Outline each blood parasite and name the species.
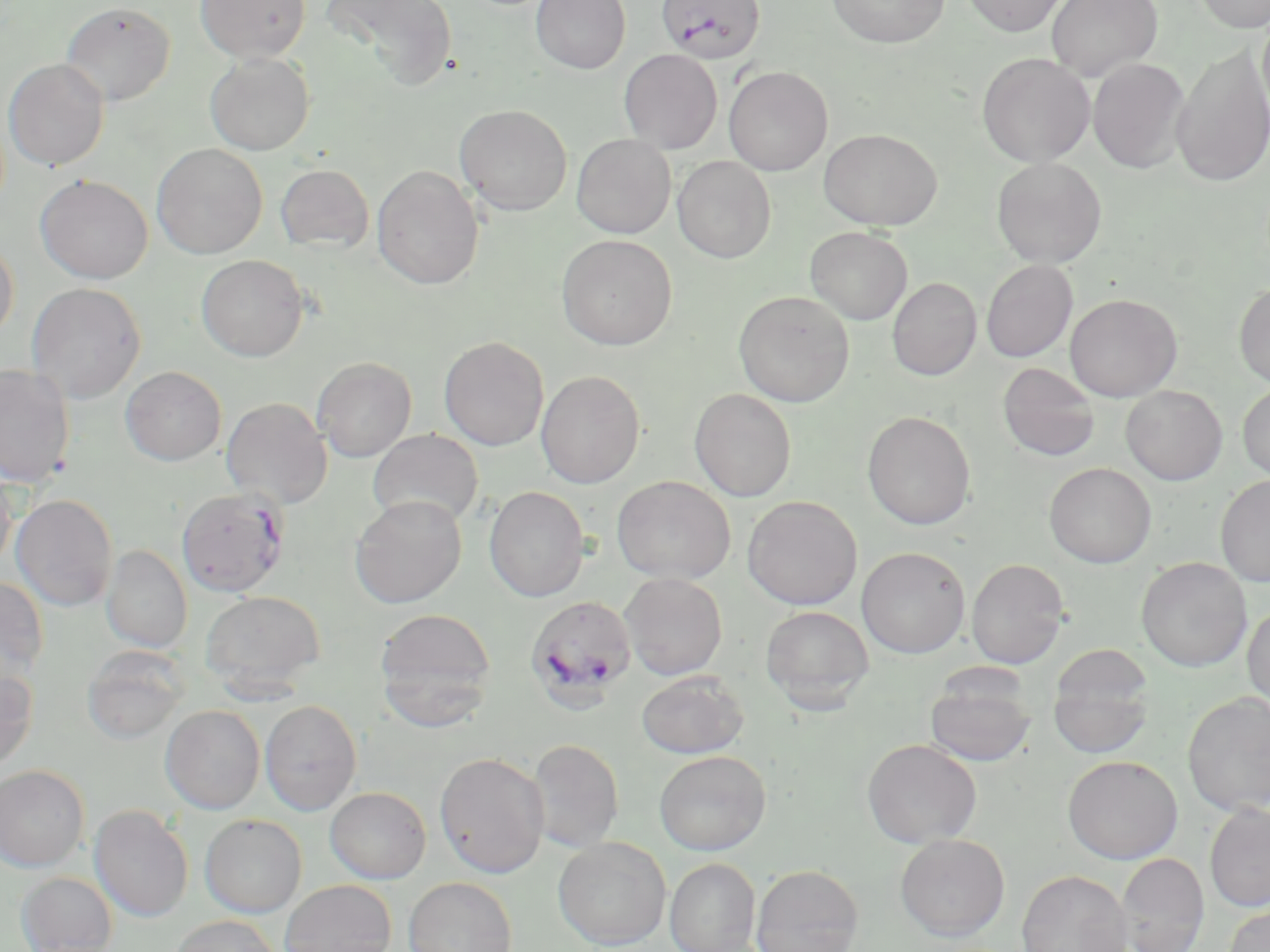
Approximate bounding boxes as [x1, y1, x2, y2] in pixels.
Plasmodium falciparum-infected red blood cells: [656, 0, 764, 63], [176, 487, 290, 597], [525, 595, 636, 712].
No Plasmodium ovale, Plasmodium malariae, Plasmodium vivax, Babesia divergens, or Trypanosoma brucei observed.

Uninfected red blood cell locations: [195, 0, 311, 62], [323, 0, 458, 90], [531, 0, 631, 73], [827, 0, 950, 49], [959, 0, 1070, 37], [1046, 0, 1163, 82], [1192, 0, 1270, 32], [60, 2, 175, 106], [1258, 11, 1270, 126], [1171, 44, 1270, 188], [619, 49, 722, 153], [205, 53, 315, 156], [977, 53, 1095, 166], [3, 58, 110, 171], [1087, 58, 1191, 174], [723, 66, 832, 176], [455, 104, 572, 215], [818, 128, 942, 230], [571, 134, 675, 238], [151, 143, 267, 259], [673, 156, 776, 262], [991, 156, 1107, 267], [275, 164, 375, 254], [372, 165, 484, 290], [35, 174, 154, 284], [805, 226, 913, 325], [556, 234, 677, 350], [0, 237, 19, 344], [196, 254, 309, 361], [981, 259, 1078, 362], [887, 277, 981, 381], [1234, 281, 1270, 388], [26, 282, 146, 404], [733, 290, 854, 407], [1065, 293, 1182, 402], [438, 336, 549, 451], [311, 356, 417, 462], [997, 362, 1101, 462], [0, 364, 76, 487], [120, 366, 227, 466], [536, 370, 645, 488], [1237, 381, 1270, 482], [1120, 385, 1227, 485], [689, 388, 797, 502], [221, 397, 332, 508], [862, 411, 976, 530], [367, 429, 484, 528], [1044, 462, 1156, 567], [0, 464, 17, 573], [1216, 475, 1270, 588], [611, 476, 735, 584], [484, 486, 589, 602], [11, 494, 118, 611], [349, 495, 467, 608], [743, 496, 862, 610], [101, 545, 192, 652], [857, 546, 970, 658], [1135, 557, 1252, 672], [966, 558, 1070, 668], [619, 572, 727, 680], [0, 576, 49, 683], [200, 590, 325, 695], [1242, 601, 1270, 713], [760, 605, 874, 712], [374, 608, 497, 725], [81, 645, 189, 745], [1048, 646, 1154, 757], [0, 665, 38, 771], [636, 670, 749, 758], [924, 673, 1035, 767], [1182, 692, 1269, 816], [260, 700, 362, 815], [160, 705, 265, 814], [527, 738, 624, 853], [862, 738, 982, 848], [653, 750, 771, 855], [434, 751, 550, 878], [1063, 755, 1182, 863], [0, 765, 89, 872], [325, 787, 430, 884], [1204, 803, 1270, 912], [88, 804, 193, 922], [200, 814, 307, 917], [895, 834, 1009, 941], [553, 837, 671, 950], [1116, 852, 1209, 952], [665, 858, 760, 952], [750, 864, 863, 952], [1017, 869, 1133, 952], [16, 871, 117, 952], [403, 877, 518, 952], [280, 880, 396, 952], [1223, 902, 1270, 952], [169, 915, 284, 952]. Slide-level diagnosis: Plasmodium falciparum. Thin blood smear. Image is 1270×952 pixels. Light microscopy. Captured at 1000x magnification. May-Grünwald-Giemsa stain. Single field of view.